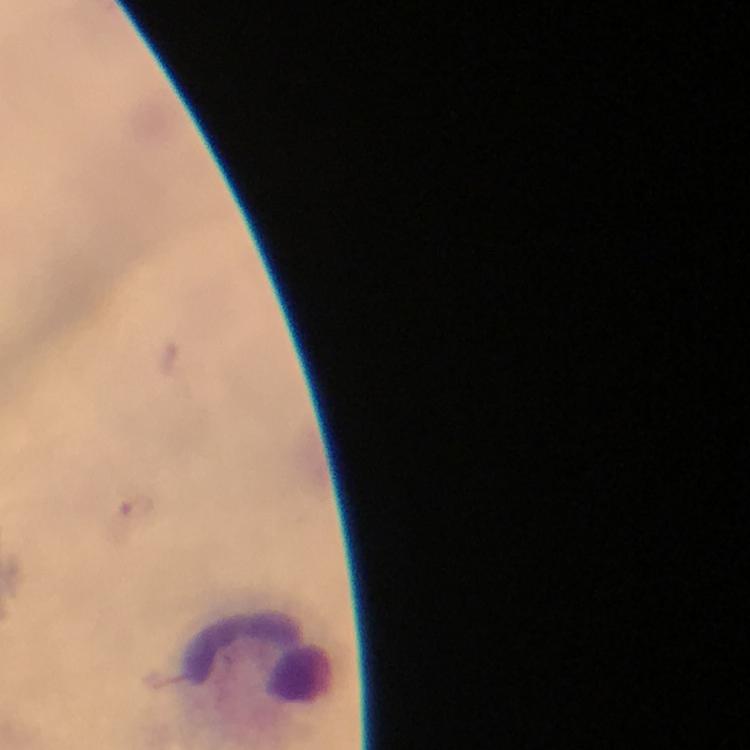
{
  "magnification": "100x",
  "image_size": "750×750 pixels",
  "capture": "smartphone camera through the microscope",
  "preparation": "thick blood film",
  "stain": "Giemsa",
  "context": "from a malaria diagnostic workup",
  "cropped_from": "a single field of view",
  "immersion_oil": "used",
  "plasmodium_parasite_locations": "approximate centers as [x, y] in pixels: [136, 507]"
}